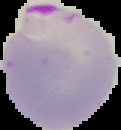
image_size: 121×130 pixels
image_type: segmented cell region on a black background
preparation: thin blood smear
malaria_status: parasitized